Assess for parasitized red blood cells.
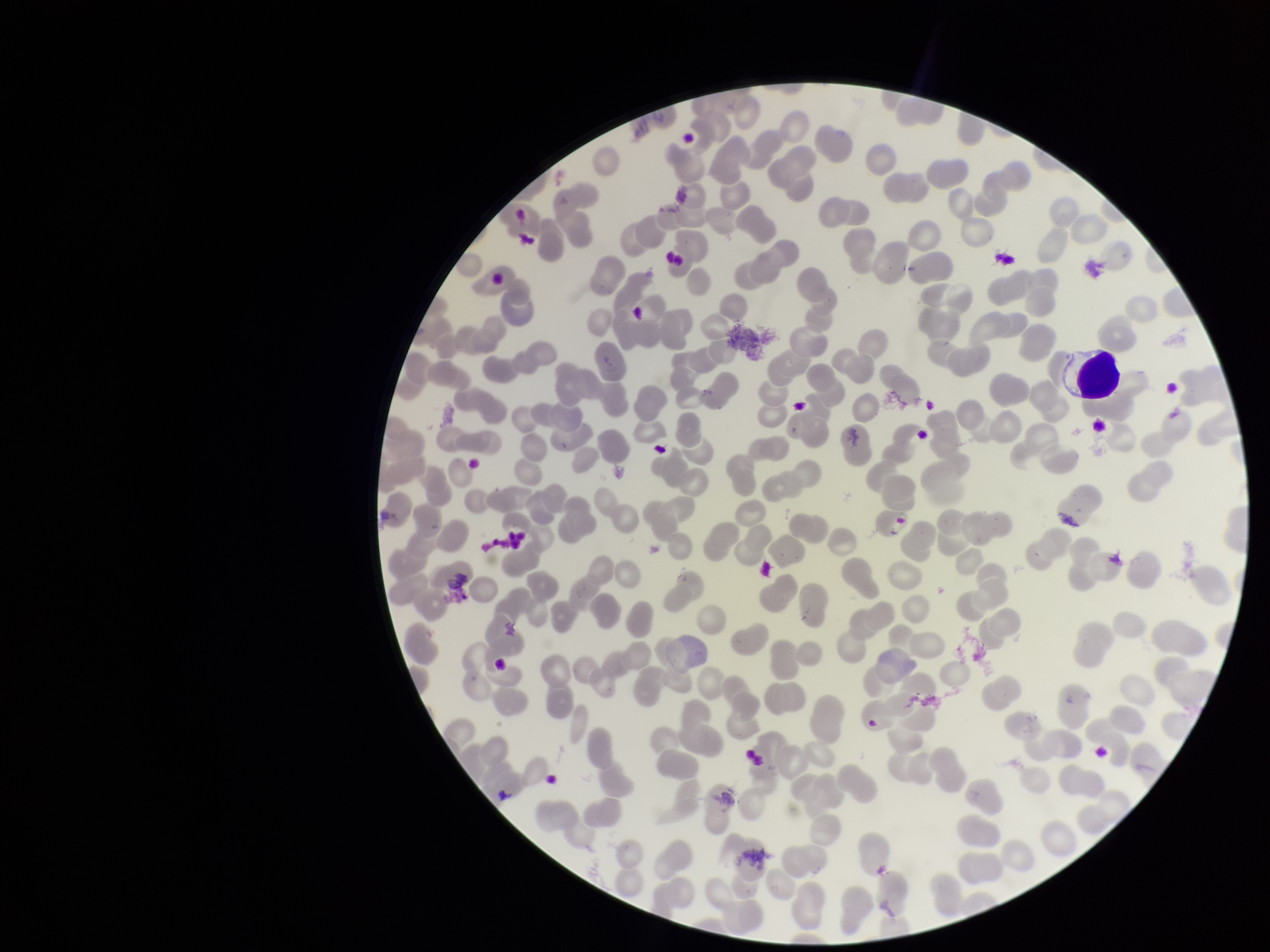
None seen.

{
  "red_blood_cell_count": 227,
  "stain": "Giemsa",
  "field_of_view": "one from this slide",
  "image_size": "1270×952 pixels",
  "patient_malaria_status": "negative",
  "preparation": "thin smear",
  "parasitized_red_blood_cell_count": 0,
  "capture": "smartphone photograph through the microscope eyepiece"
}